Locate every blood parasite and identify its species.
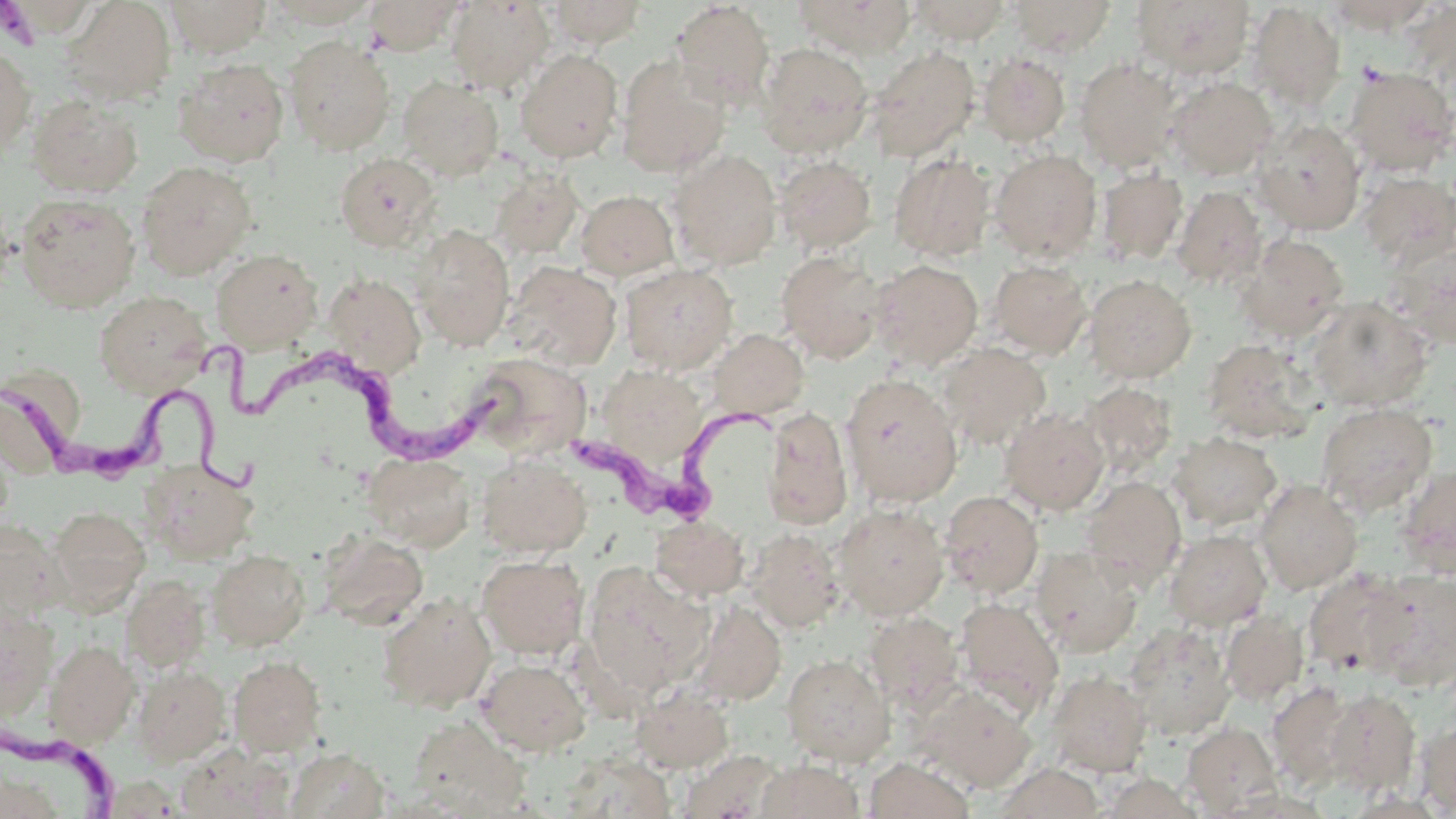
Approximate bounding boxes as (x1,y1)-(x2,y2) corner pairs in pixels.
Trypanosoma brucei: (190,336)-(509,462), (7,361)-(265,513), (572,399)-(803,522), (0,726)-(120,818).
No Plasmodium falciparum, Plasmodium ovale, Plasmodium malariae, Plasmodium vivax, or Babesia divergens observed.

Summary:
  - Platelet locations: (0,3)-(32,41)
  - Uninfected red blood cell locations: (61,0)-(176,104), (164,0)-(272,57), (364,0)-(463,55), (545,0)-(649,49), (795,0)-(917,59), (910,0)-(1011,45), (1008,0)-(1117,56), (1131,0)-(1256,79), (261,1)-(383,28), (445,1)-(555,94), (670,1)-(775,107), (1323,1)-(1439,34), (1247,2)-(1346,112), (284,36)-(395,156), (757,43)-(873,158), (0,45)-(36,158), (866,45)-(980,162), (515,49)-(623,163), (979,52)-(1070,146), (616,56)-(731,177), (1075,57)-(1183,172), (173,58)-(290,167), (1343,66)-(1456,175), (398,76)-(504,180), (1165,76)-(1277,179), (27,94)-(144,197), (1252,119)-(1366,234), (669,149)-(783,270), (990,149)-(1102,263), (334,152)-(441,252), (889,153)-(995,262), (775,155)-(877,254), (136,160)-(257,279), (489,167)-(585,259), (1095,167)-(1188,266), (1359,171)-(1456,265), (1171,185)-(1267,289), (575,190)-(680,280), (16,194)-(140,312), (411,225)-(515,351), (1235,234)-(1349,340), (1386,239)-(1456,349), (210,248)-(323,352), (775,250)-(886,363), (871,259)-(984,370), (503,260)-(623,372), (987,260)-(1092,359), (620,263)-(738,374), (322,273)-(426,378), (1084,274)-(1196,383), (92,290)-(212,396), (1307,297)-(1433,411), (708,329)-(809,420), (1202,339)-(1317,443), (937,342)-(1052,450), (465,351)-(593,459), (596,365)-(708,471), (840,373)-(963,508), (0,379)-(73,474), (1081,381)-(1178,476), (1316,402)-(1438,515), (761,407)-(854,530), (1000,407)-(1110,515), (0,428)-(16,529), (1169,432)-(1282,530), (364,453)-(475,551), (477,454)-(591,557), (140,457)-(260,563), (1399,464)-(1456,577), (1080,475)-(1187,589), (1254,478)-(1363,594), (939,491)-(1043,599), (834,503)-(949,620), (47,506)-(151,611), (650,516)-(750,600), (0,520)-(63,624), (745,528)-(846,632), (1164,529)-(1272,631), (316,531)-(428,630), (1031,546)-(1144,658), (207,550)-(310,650), (217,551)-(314,757), (477,554)-(589,659), (582,562)-(712,696), (1303,569)-(1412,679), (1364,569)-(1456,690), (121,574)-(212,674), (377,592)-(496,711), (955,597)-(1064,717), (692,600)-(786,706), (0,607)-(58,721), (1220,610)-(1309,705), (863,611)-(964,713), (1122,622)-(1235,739), (44,639)-(139,747), (782,654)-(894,766), (228,655)-(326,757), (477,657)-(591,756), (132,664)-(231,765), (1045,670)-(1152,777), (1267,680)-(1356,789), (915,684)-(1036,792), (630,685)-(734,773), (1325,687)-(1422,795), (407,715)-(529,817), (1416,719)-(1456,816), (1182,722)-(1281,816), (176,746)-(295,819), (286,747)-(390,819), (677,750)-(786,818), (864,758)-(976,818), (756,760)-(864,818), (993,762)-(1105,819), (1097,771)-(1206,818)
  - Slide-level diagnosis: Trypanosoma brucei
  - Field of view: one of a larger specimen
  - Image size: 1456×819 pixels
  - Preparation: thin blood film
  - Stain: May-Grünwald-Giemsa
  - Magnification: 1000x
  - Modality: optical microscopy